Comment on the morphology of the erythrocytes.
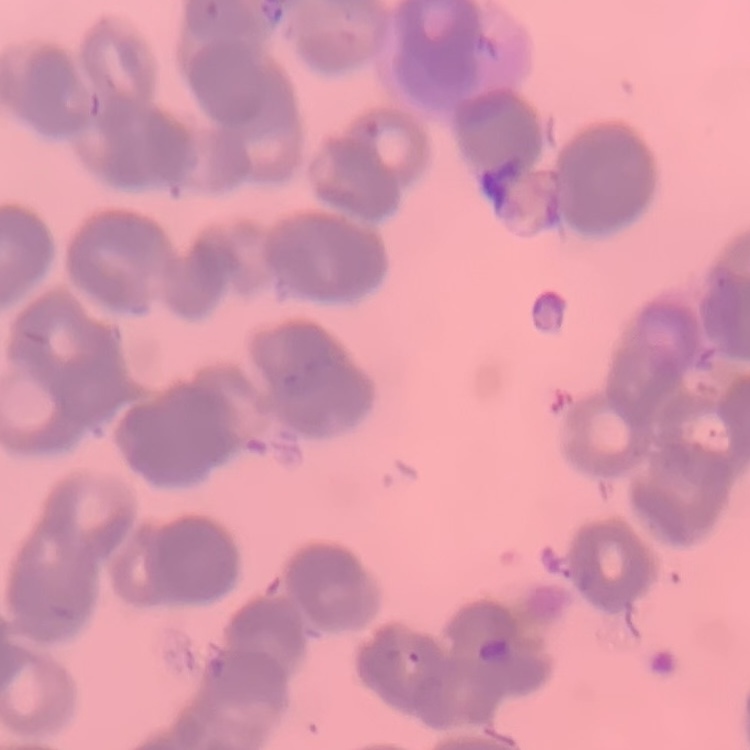

They show rouleaux formation.

Summary:
  - Image type: one tile cut from a larger photomicrograph
  - Preparation: thin peripheral smear
  - Stain: Field's or Giemsa